Report the malaria status of this cell.
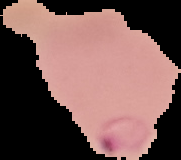

Parasitized.

Summary:
  - Image size: 181×160 pixels
  - Preparation: thin blood film
  - Image type: cell region segmented out of the field of view; surrounding area masked to black